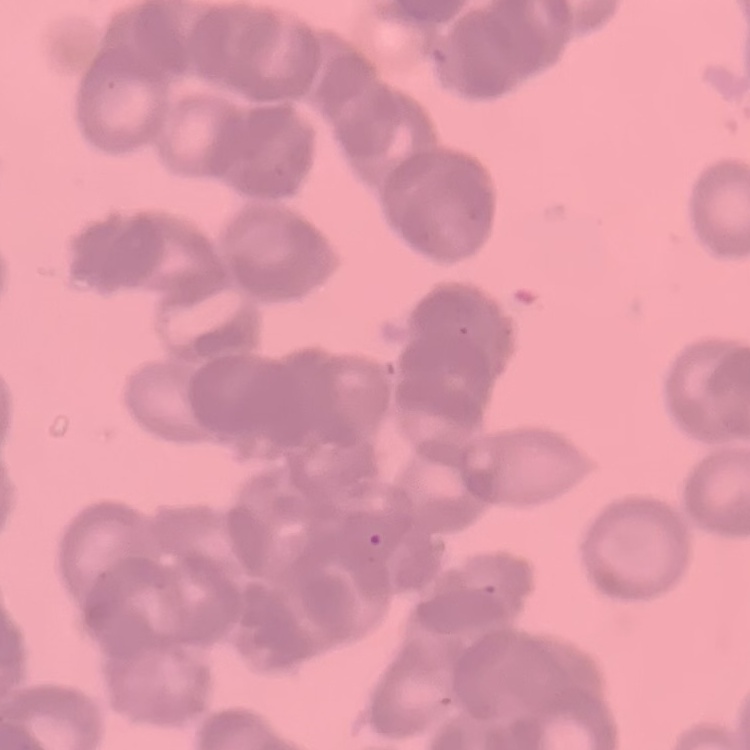

Summary:
  - Red blood cell morphology: rouleaux formation
  - Preparation: thin blood smear
  - Image type: square crop of a larger photomicrograph
  - Stain: Field's or Giemsa